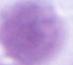
An erythrocyte is seen. Micrograph. 1000x magnification.